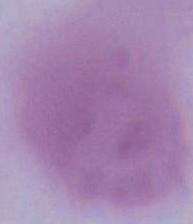

Summary:
  - Magnification: 1000x
  - Identification: erythrocyte
  - Modality: photomicrograph